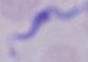

magnification = 1000x
modality = photomicrograph
identification = trypanosome